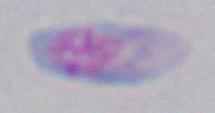 Photomicrograph. Toxoplasma gondii is seen. 1000x magnification.